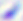

Toxoplasma gondii is shown. Captured at 400x magnification. Photomicrograph.